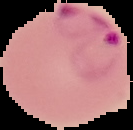
Summary:
  - Malaria status: parasitized
  - Preparation: thin blood smear
  - Image size: 133×130 pixels
  - Image type: cell region segmented out of the field of view; surrounding area masked to black